Name the parasite shown.
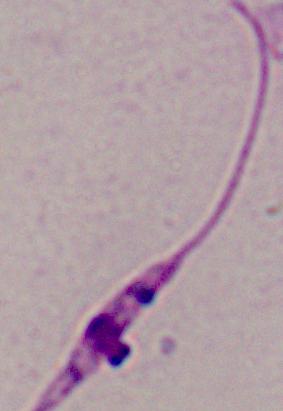

Leishmania.

Micrograph. 1000x magnification.